Classify this cell by malaria status.
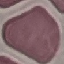
It is uninfected.

Summary:
  - Image type: cell patch, automatically extracted from a larger field of view and resized to 64 × 64 pixels
  - Preparation: thin smear
  - Stain: Giemsa
  - Capture: smartphone camera at the microscope eyepiece